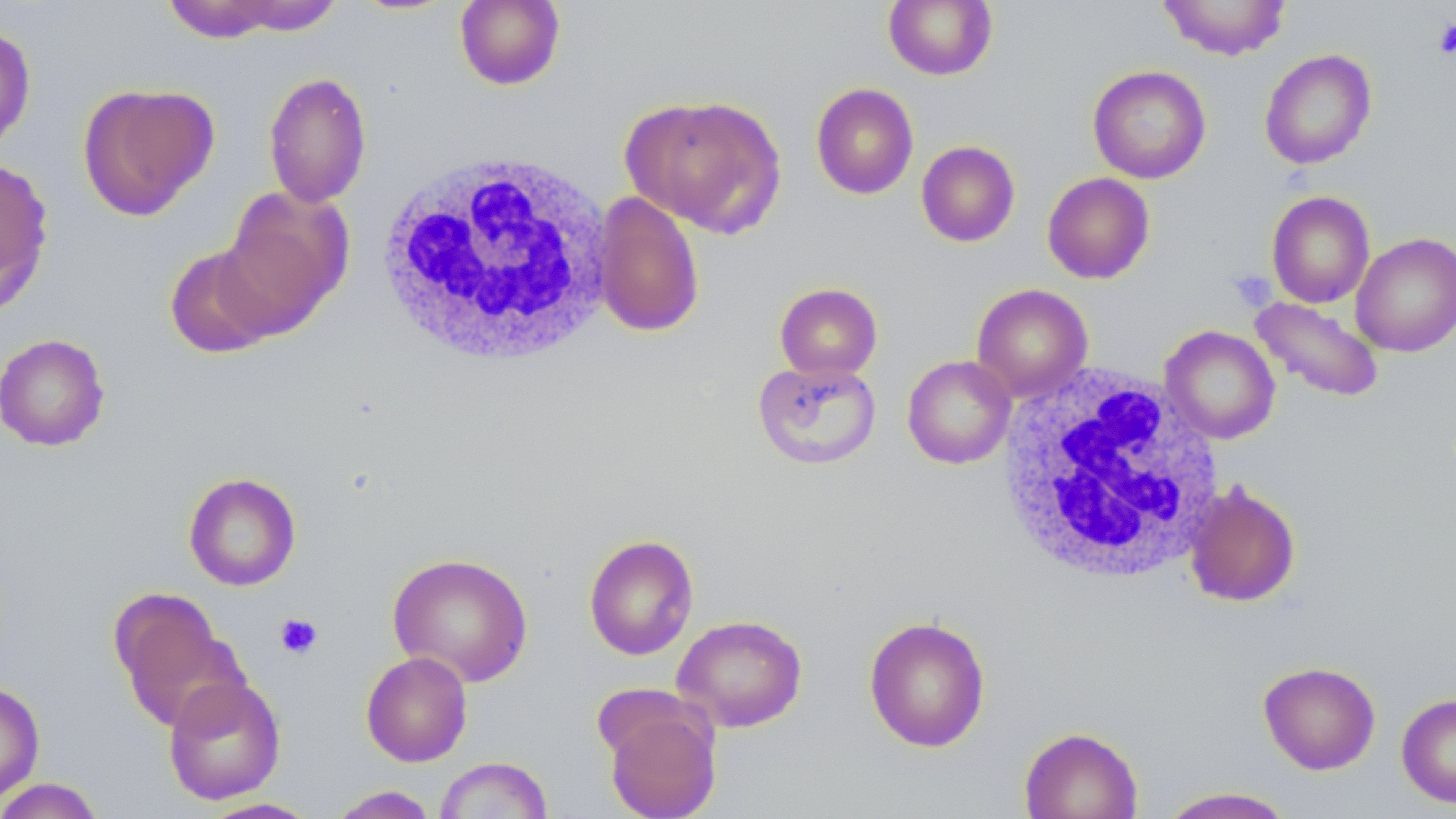
slide-level diagnosis = negative for blood parasites
platelet locations = approximate bounding boxes as named x1/y1/x2/y2 corners in pixels: (x1=1433, y1=18, x2=1456, y2=60), (x1=1228, y1=268, x2=1276, y2=311), (x1=275, y1=613, x2=323, y2=659)
image size = 1456×819 pixels
field of view = one of a larger specimen
magnification = 1000x
white blood cell locations = approximate bounding boxes as named x1/y1/x2/y2 corners in pixels: (x1=373, y1=149, x2=619, y2=369), (x1=995, y1=366, x2=1228, y2=585)
uninfected red blood cell locations = approximate bounding boxes as named x1/y1/x2/y2 corners in pixels: (x1=210, y1=0, x2=346, y2=36), (x1=455, y1=0, x2=566, y2=90), (x1=1158, y1=0, x2=1292, y2=60), (x1=158, y1=1, x2=301, y2=42), (x1=883, y1=1, x2=998, y2=80), (x1=0, y1=22, x2=37, y2=154), (x1=1259, y1=49, x2=1377, y2=170), (x1=1087, y1=65, x2=1211, y2=184), (x1=263, y1=71, x2=372, y2=208), (x1=77, y1=82, x2=219, y2=220), (x1=810, y1=82, x2=919, y2=199), (x1=621, y1=93, x2=786, y2=237), (x1=916, y1=140, x2=1020, y2=247), (x1=0, y1=158, x2=54, y2=313), (x1=1042, y1=172, x2=1156, y2=284), (x1=219, y1=184, x2=353, y2=333), (x1=1266, y1=190, x2=1375, y2=308), (x1=592, y1=191, x2=705, y2=338), (x1=1350, y1=232, x2=1456, y2=357), (x1=164, y1=245, x2=278, y2=359), (x1=775, y1=282, x2=883, y2=380), (x1=971, y1=284, x2=1092, y2=402), (x1=1250, y1=297, x2=1385, y2=403), (x1=1160, y1=325, x2=1281, y2=444), (x1=0, y1=333, x2=110, y2=451), (x1=902, y1=355, x2=1016, y2=469), (x1=753, y1=358, x2=881, y2=470), (x1=184, y1=472, x2=302, y2=591), (x1=1184, y1=481, x2=1301, y2=607), (x1=583, y1=534, x2=699, y2=661), (x1=387, y1=552, x2=533, y2=687), (x1=108, y1=588, x2=245, y2=732), (x1=671, y1=614, x2=808, y2=732), (x1=863, y1=615, x2=991, y2=753), (x1=361, y1=651, x2=473, y2=767), (x1=1258, y1=661, x2=1381, y2=774), (x1=162, y1=675, x2=287, y2=805), (x1=0, y1=680, x2=45, y2=806), (x1=1396, y1=692, x2=1456, y2=808), (x1=603, y1=700, x2=721, y2=819), (x1=1019, y1=726, x2=1143, y2=818), (x1=434, y1=756, x2=553, y2=818), (x1=0, y1=778, x2=106, y2=819), (x1=327, y1=785, x2=439, y2=818), (x1=1157, y1=786, x2=1296, y2=818), (x1=197, y1=797, x2=322, y2=818)
stain = May-Grünwald-Giemsa
preparation = thin blood smear
modality = light microscopy